Name the parasite shown.
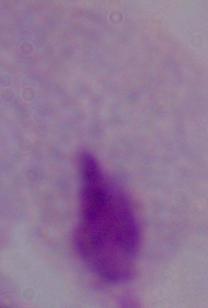

This is a trichomonad.

Summary:
  - Magnification: 1000x
  - Modality: micrograph